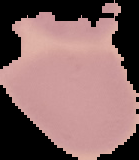
Summary:
  - Malaria status: uninfected
  - Preparation: thin blood smear
  - Image size: 139×160 pixels
  - Image type: cell region segmented out of the field of view; surrounding area masked to black